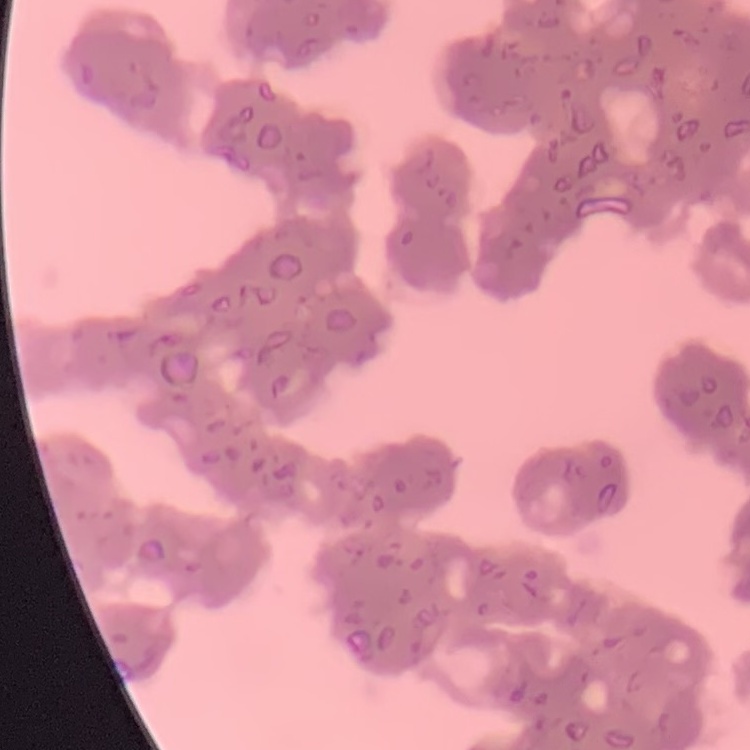
{
  "erythrocyte_morphology": "rouleaux formation",
  "image_type": "one tile cut from a larger photomicrograph",
  "stain": "Field's or Giemsa",
  "preparation": "thin peripheral smear"
}